Report the malaria status of this cell.
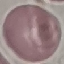

Uninfected.

Acquired by smartphone through the microscope eyepiece. Thin blood film. Automatically extracted cell patch, resized to 64 × 64 pixels. Giemsa-stained preparation.